Assess this cell for malaria.
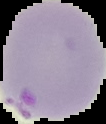
It is parasitized.

Summary:
  - Image type: segmented cell region with the area outside set to black
  - Preparation: thin blood film
  - Image size: 106×124 pixels